Assess this cell for malaria.
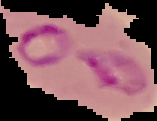

It is parasitized.

image size = 157×121 pixels
image type = segmented cell region with the area outside set to black
preparation = thin blood smear